Locate and identify every blood parasite.
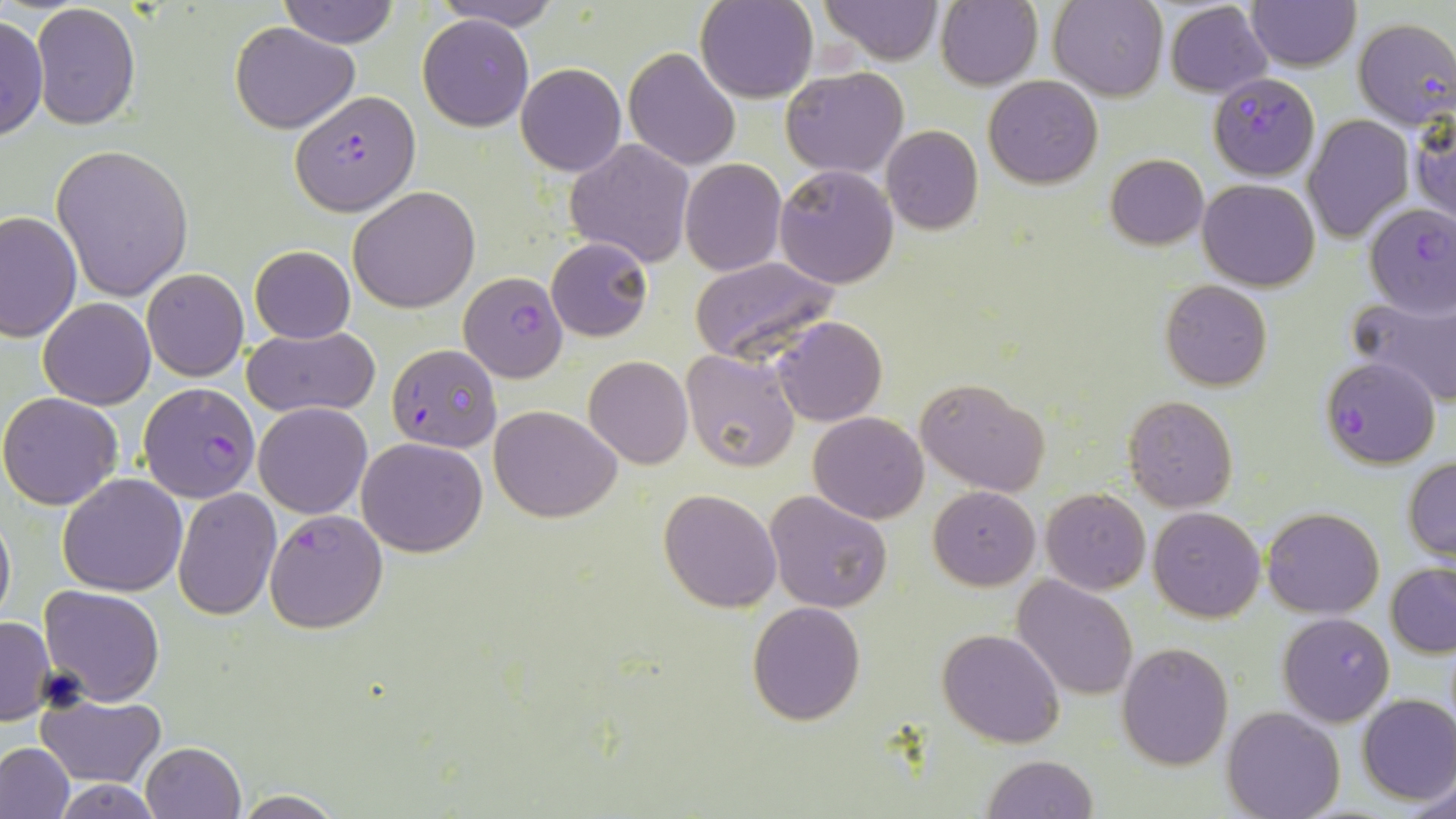
Approximate bounding boxes as (x1,y1)-(x2,y2) corner pairs in pixels.
Plasmodium falciparum-infected red blood cells: (1352,18)-(1456,129), (1212,75)-(1320,181), (292,89)-(420,214), (1365,203)-(1456,317), (459,271)-(568,383), (386,343)-(502,453), (1319,356)-(1440,469), (138,383)-(261,502), (264,510)-(388,632), (1277,612)-(1394,727).
No Plasmodium ovale, Plasmodium malariae, Plasmodium vivax, Babesia divergens, or Trypanosoma brucei observed.

Uninfected red blood cell locations: (278,0)-(401,48), (431,0)-(564,30), (696,0)-(818,102), (818,0)-(944,65), (936,0)-(1043,90), (1048,0)-(1167,100), (1164,1)-(1272,96), (1247,1)-(1360,71), (30,4)-(142,131), (0,13)-(47,141), (418,13)-(533,131), (230,21)-(359,134), (622,47)-(741,172), (516,63)-(627,177), (782,67)-(909,179), (983,76)-(1104,188), (1410,109)-(1455,230), (1303,114)-(1412,243), (881,125)-(984,234), (565,138)-(694,267), (50,144)-(194,301), (1104,153)-(1209,250), (680,157)-(786,276), (775,165)-(899,290), (1197,178)-(1321,290), (349,187)-(480,313), (0,209)-(81,343), (546,235)-(654,341), (250,245)-(355,345), (688,256)-(842,365), (142,269)-(249,380), (1159,280)-(1271,390), (1348,295)-(1456,404), (39,297)-(155,409), (773,316)-(888,426), (244,326)-(379,417), (680,348)-(801,474), (584,356)-(692,468), (917,378)-(1050,497), (0,392)-(124,511), (1123,395)-(1238,512), (253,402)-(372,519), (490,405)-(621,522), (808,412)-(929,524), (357,437)-(489,557), (1404,456)-(1456,560), (58,474)-(187,595), (928,486)-(1040,589), (173,487)-(281,619), (1041,487)-(1150,594), (659,488)-(782,613), (765,491)-(893,613), (0,505)-(15,631), (1148,507)-(1266,622), (1262,507)-(1383,617), (1387,563)-(1456,658), (1012,575)-(1138,700), (39,584)-(165,705), (747,602)-(866,725), (0,615)-(54,725), (938,628)-(1064,748), (1117,642)-(1233,769), (37,694)-(165,787), (1358,694)-(1456,804), (1221,705)-(1344,819), (0,740)-(74,819), (139,741)-(247,819), (982,753)-(1098,819), (1409,770)-(1456,819), (48,779)-(169,817), (230,791)-(348,819). Slide-level diagnosis: Plasmodium falciparum. Captured at 1000x magnification. Light microscopy. Thin blood film. Image is 1456×819 pixels. One field of a larger specimen. May-Grünwald-Giemsa stain.